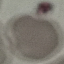 Malaria status: uninfected. Cell patch, automatically extracted from a larger field of view and resized to 64 × 64 pixels. Thin smear of blood. Photographed with a smartphone camera at the microscope eyepiece. Giemsa stain.